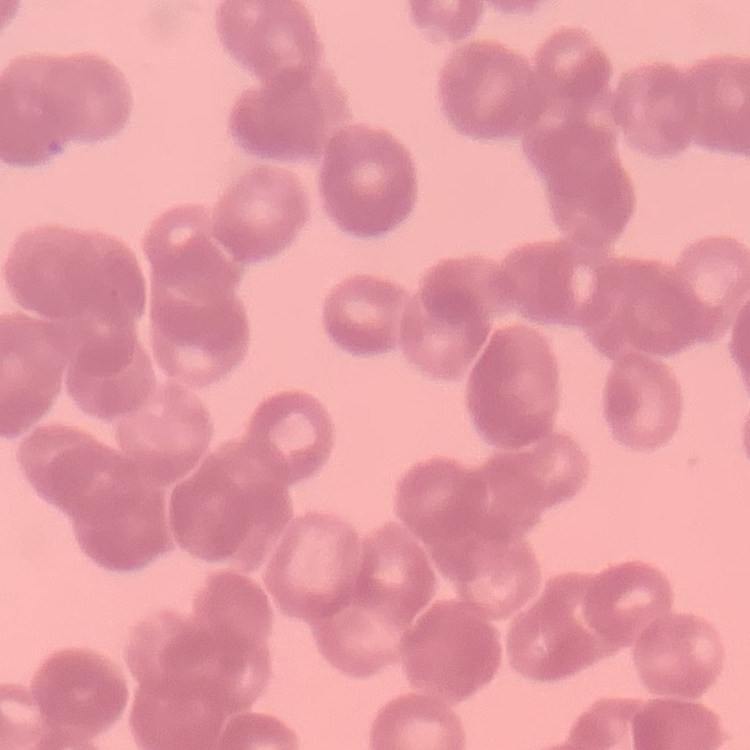
erythrocyte morphology = rouleaux formation
preparation = thin blood smear
image type = one tile cut from a larger photomicrograph
stain = Field's or Giemsa